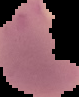

Summary:
  - Image type: cell region segmented out of the field of view; surrounding area masked to black
  - Image size: 79×97 pixels
  - Preparation: thin blood smear
  - Malaria status: parasitized